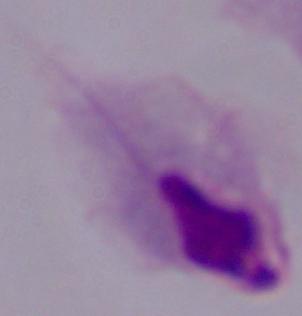
Summary:
  - Identification: trichomonad
  - Magnification: 1000x
  - Modality: photomicrograph